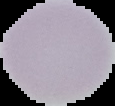

preparation: thin blood film
image_size: 115×106 pixels
malaria_status: uninfected
image_type: segmented cell region with the area outside set to black